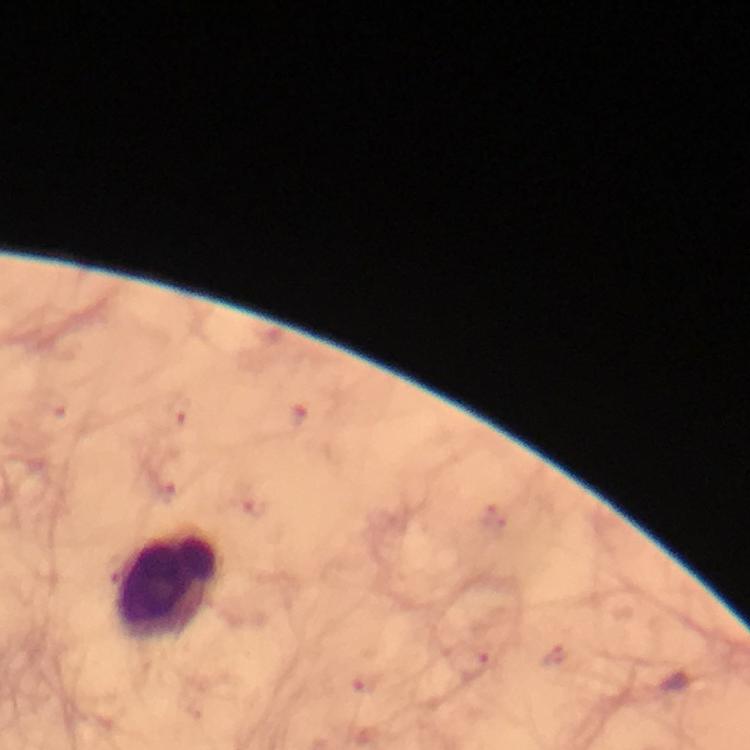
{
  "plasmodium_parasites": "none seen",
  "image_size": "750×750 pixels",
  "capture": "smartphone photograph through a microscope",
  "stain": "Giemsa",
  "immersion_oil": "used",
  "preparation": "thick smear",
  "context": "from a malaria diagnostic workup",
  "cropped_from": "a single field of view",
  "leukocyte_locations": "approximate centers as {x, y} in pixels: {165, 584}",
  "magnification": "100x"
}